Comment on the morphology of the erythrocytes.
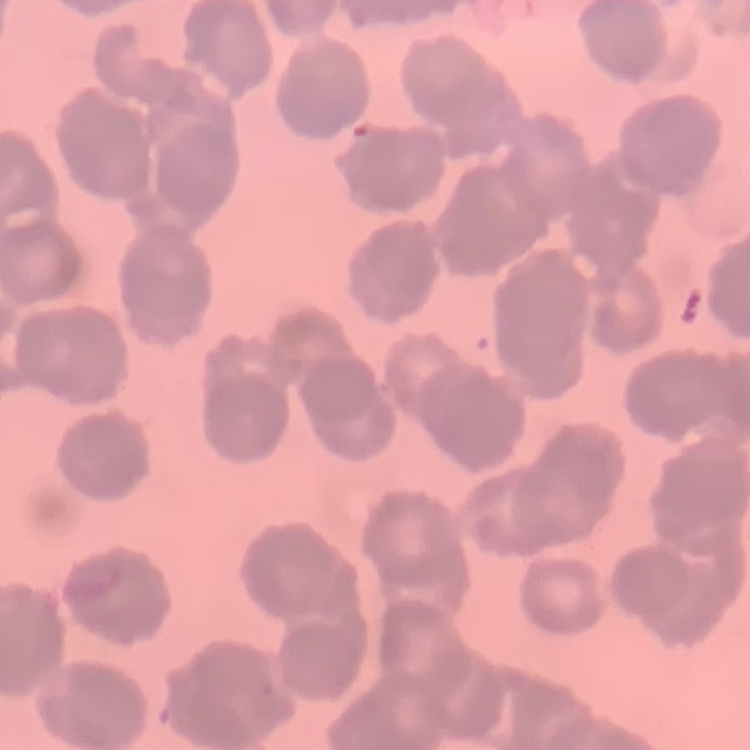

They show rouleaux formation.

{
  "preparation": "thin peripheral smear",
  "image_type": "square crop of a larger photomicrograph",
  "stain": "Field's or Giemsa"
}